Classify this cell by malaria status.
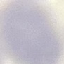
It is uninfected.

preparation: thin smear
image_type: cell patch, automatically extracted from a larger field of view and resized to 64 × 64 pixels
capture: smartphone through the microscope eyepiece
stain: Giemsa